Report the malaria status of this cell.
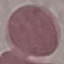

It is uninfected.

Thin blood smear. Cell patch, automatically extracted from a larger field of view and resized to 64 × 64 pixels. Giemsa-stained preparation. Photographed with a smartphone camera at the microscope eyepiece.